Outline each blood parasite and name the species.
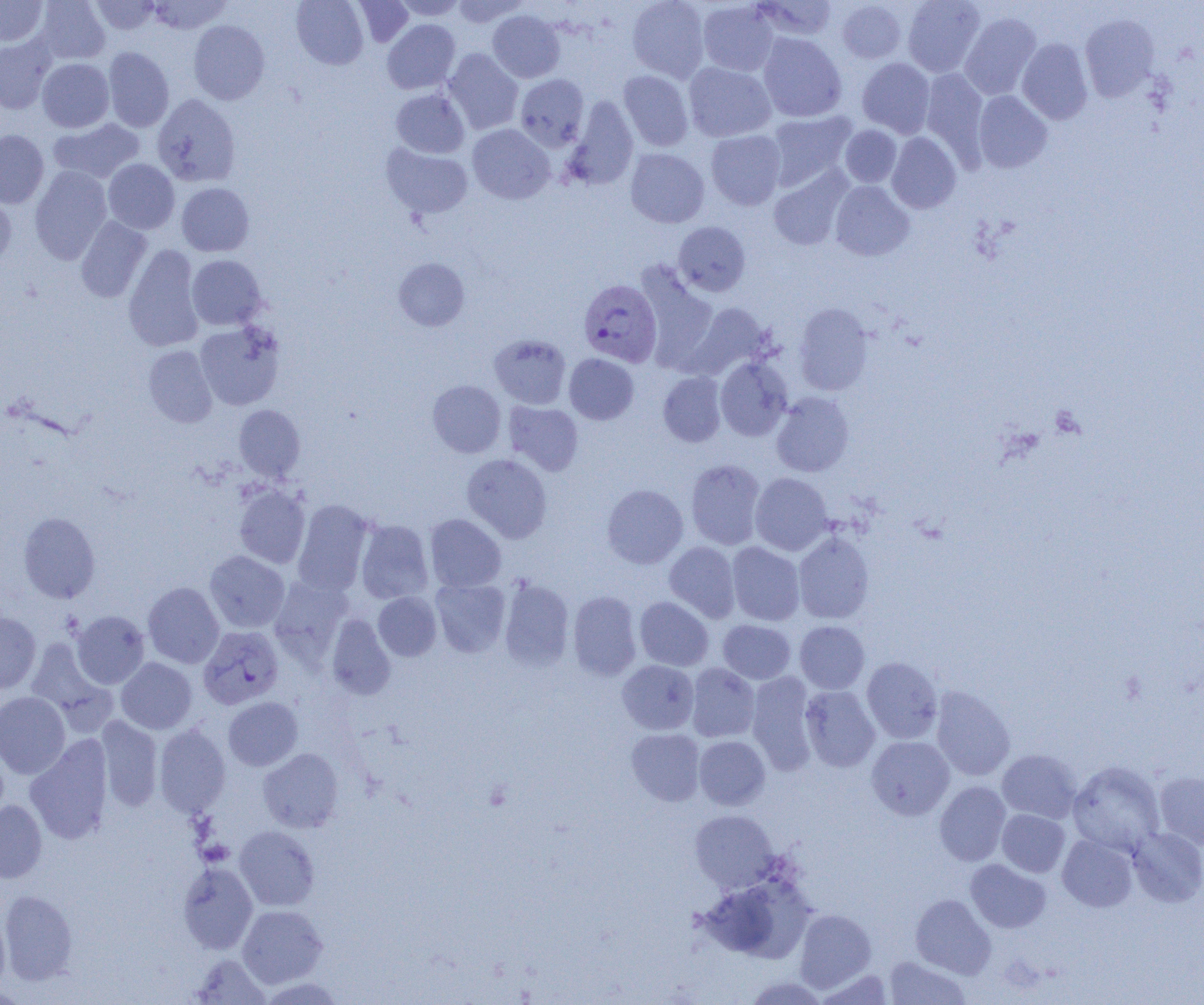

Approximate bounding boxes as named x1/y1/x2/y2 corners in pixels.
Plasmodium vivax-infected red blood cells: (x1=578, y1=278, x2=662, y2=366), (x1=198, y1=626, x2=284, y2=709).
No Plasmodium falciparum, Plasmodium ovale, Plasmodium malariae, Babesia divergens, or Trypanosoma brucei observed.

Summary:
  - Uninfected red blood cell locations: (x1=0, y1=0, x2=47, y2=46), (x1=34, y1=0, x2=110, y2=64), (x1=90, y1=0, x2=160, y2=34), (x1=146, y1=0, x2=232, y2=34), (x1=292, y1=0, x2=368, y2=69), (x1=393, y1=0, x2=467, y2=20), (x1=451, y1=0, x2=529, y2=27), (x1=627, y1=0, x2=710, y2=82), (x1=753, y1=0, x2=838, y2=42), (x1=902, y1=0, x2=985, y2=77), (x1=352, y1=1, x2=414, y2=47), (x1=697, y1=1, x2=780, y2=76), (x1=837, y1=1, x2=906, y2=63), (x1=487, y1=10, x2=565, y2=83), (x1=959, y1=12, x2=1041, y2=100), (x1=1079, y1=13, x2=1160, y2=101), (x1=382, y1=19, x2=460, y2=93), (x1=188, y1=20, x2=270, y2=105), (x1=758, y1=33, x2=846, y2=122), (x1=0, y1=36, x2=57, y2=114), (x1=1017, y1=38, x2=1093, y2=124), (x1=103, y1=47, x2=174, y2=132), (x1=443, y1=48, x2=523, y2=134), (x1=37, y1=58, x2=114, y2=132), (x1=857, y1=58, x2=936, y2=138), (x1=683, y1=62, x2=776, y2=141), (x1=920, y1=68, x2=989, y2=160), (x1=619, y1=70, x2=693, y2=151), (x1=515, y1=74, x2=589, y2=151), (x1=391, y1=88, x2=470, y2=158), (x1=973, y1=90, x2=1052, y2=173), (x1=152, y1=94, x2=241, y2=187), (x1=564, y1=96, x2=638, y2=190), (x1=765, y1=110, x2=857, y2=190), (x1=48, y1=118, x2=144, y2=184), (x1=467, y1=124, x2=555, y2=204), (x1=839, y1=125, x2=901, y2=187), (x1=0, y1=130, x2=49, y2=208), (x1=706, y1=130, x2=786, y2=210), (x1=886, y1=132, x2=961, y2=213), (x1=381, y1=143, x2=472, y2=219), (x1=625, y1=148, x2=709, y2=228), (x1=103, y1=158, x2=179, y2=234), (x1=29, y1=166, x2=112, y2=263), (x1=769, y1=168, x2=851, y2=251), (x1=830, y1=180, x2=914, y2=261), (x1=176, y1=183, x2=254, y2=256), (x1=0, y1=191, x2=17, y2=268), (x1=76, y1=216, x2=151, y2=302), (x1=673, y1=221, x2=751, y2=296), (x1=123, y1=245, x2=204, y2=352), (x1=187, y1=255, x2=266, y2=330), (x1=393, y1=258, x2=470, y2=331), (x1=635, y1=262, x2=718, y2=370), (x1=690, y1=302, x2=775, y2=378), (x1=793, y1=303, x2=874, y2=396), (x1=195, y1=321, x2=285, y2=410), (x1=489, y1=334, x2=571, y2=409), (x1=143, y1=345, x2=217, y2=427), (x1=564, y1=354, x2=638, y2=424), (x1=715, y1=356, x2=793, y2=441), (x1=657, y1=371, x2=727, y2=447), (x1=427, y1=380, x2=506, y2=458), (x1=771, y1=391, x2=854, y2=477), (x1=503, y1=401, x2=583, y2=475), (x1=234, y1=405, x2=306, y2=482), (x1=462, y1=454, x2=552, y2=543), (x1=686, y1=459, x2=765, y2=550), (x1=750, y1=473, x2=833, y2=555), (x1=602, y1=475, x2=764, y2=557), (x1=234, y1=484, x2=310, y2=568), (x1=602, y1=484, x2=688, y2=568), (x1=292, y1=499, x2=373, y2=595), (x1=19, y1=512, x2=100, y2=603), (x1=425, y1=514, x2=506, y2=592), (x1=355, y1=519, x2=434, y2=604), (x1=793, y1=531, x2=874, y2=624), (x1=664, y1=541, x2=741, y2=623), (x1=726, y1=542, x2=805, y2=625), (x1=205, y1=551, x2=289, y2=632), (x1=269, y1=575, x2=353, y2=664), (x1=430, y1=579, x2=511, y2=658), (x1=498, y1=579, x2=574, y2=671), (x1=143, y1=582, x2=224, y2=669), (x1=568, y1=591, x2=642, y2=680), (x1=373, y1=592, x2=441, y2=661), (x1=634, y1=597, x2=713, y2=671), (x1=71, y1=610, x2=150, y2=688), (x1=0, y1=611, x2=41, y2=693), (x1=326, y1=613, x2=395, y2=699), (x1=718, y1=619, x2=795, y2=684), (x1=795, y1=621, x2=870, y2=694), (x1=26, y1=637, x2=109, y2=721), (x1=861, y1=657, x2=943, y2=743), (x1=116, y1=658, x2=197, y2=734), (x1=617, y1=660, x2=699, y2=734), (x1=686, y1=663, x2=760, y2=742), (x1=747, y1=671, x2=818, y2=774), (x1=800, y1=685, x2=880, y2=772), (x1=931, y1=686, x2=1015, y2=781), (x1=0, y1=692, x2=70, y2=778), (x1=223, y1=697, x2=302, y2=770), (x1=96, y1=716, x2=163, y2=812), (x1=154, y1=724, x2=230, y2=818), (x1=626, y1=728, x2=705, y2=806), (x1=25, y1=736, x2=113, y2=844), (x1=694, y1=736, x2=770, y2=810), (x1=866, y1=736, x2=954, y2=820), (x1=258, y1=748, x2=343, y2=832), (x1=997, y1=749, x2=1082, y2=823), (x1=1068, y1=761, x2=1165, y2=855), (x1=1154, y1=770, x2=1204, y2=850), (x1=934, y1=781, x2=1011, y2=866), (x1=0, y1=800, x2=47, y2=883), (x1=997, y1=809, x2=1070, y2=877), (x1=690, y1=810, x2=779, y2=892), (x1=234, y1=826, x2=320, y2=911), (x1=1127, y1=827, x2=1204, y2=906), (x1=1057, y1=834, x2=1138, y2=912), (x1=966, y1=859, x2=1051, y2=933), (x1=178, y1=861, x2=258, y2=954), (x1=698, y1=878, x2=809, y2=963), (x1=0, y1=890, x2=77, y2=984), (x1=911, y1=894, x2=995, y2=978), (x1=237, y1=905, x2=327, y2=987), (x1=0, y1=906, x2=10, y2=991), (x1=795, y1=908, x2=876, y2=992), (x1=190, y1=954, x2=270, y2=1004), (x1=884, y1=956, x2=971, y2=1004), (x1=815, y1=968, x2=894, y2=1004), (x1=745, y1=975, x2=830, y2=1005), (x1=259, y1=977, x2=348, y2=1004)
  - Slide-level diagnosis: Plasmodium vivax
  - Field of view: one of a larger specimen
  - Magnification: 1000x
  - Preparation: thin blood smear
  - Image size: 1204×1005 pixels
  - Modality: optical microscopy